Point out every Plasmodium parasite and every leukocyte.
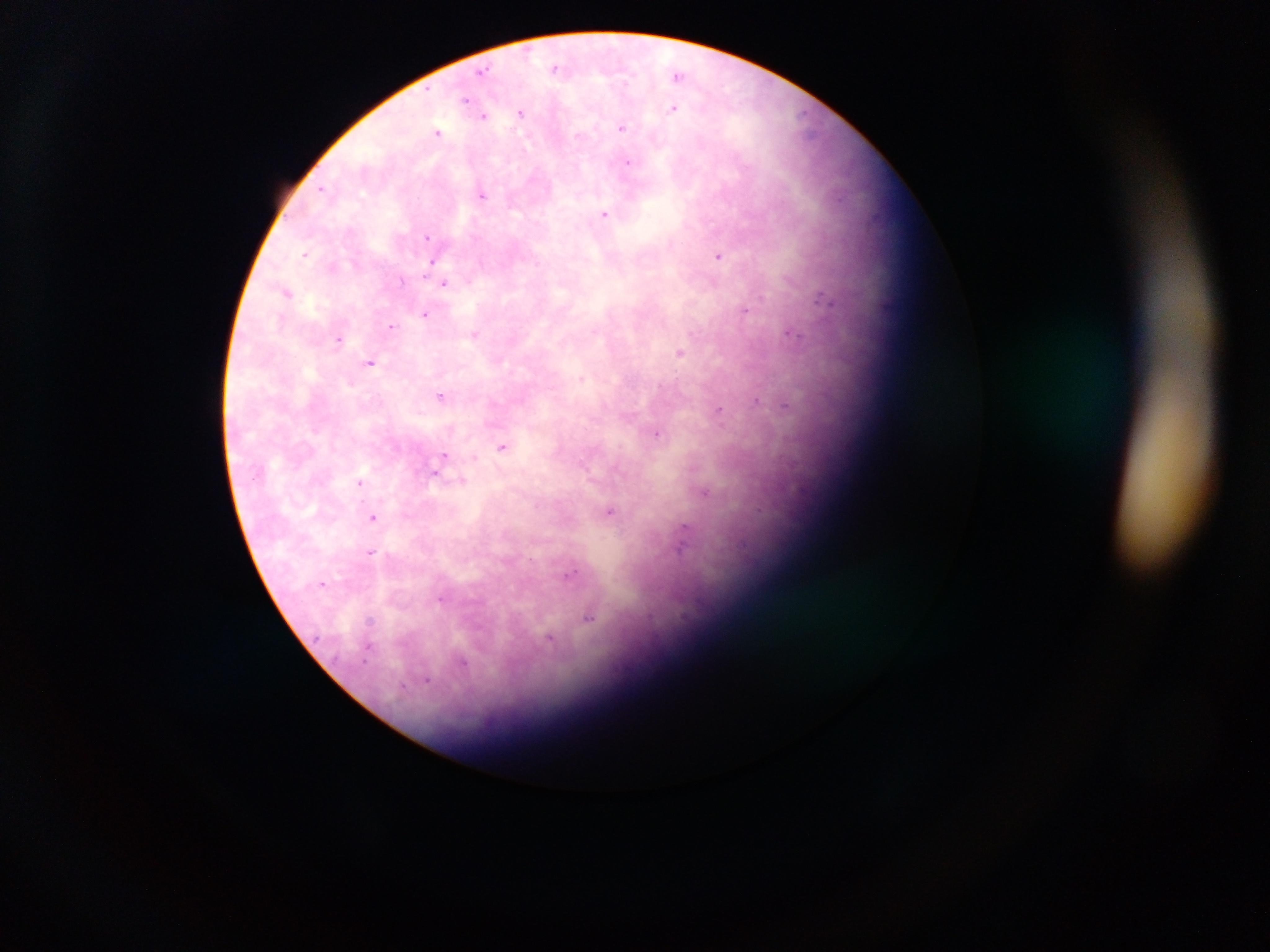

Approximate centers as {x, y} in pixels.
Plasmodium parasites: {555, 67}, {483, 71}, {677, 74}, {466, 100}, {673, 109}, {521, 113}, {484, 116}, {622, 128}, {438, 131}, {627, 161}, {323, 189}, {483, 195}, {604, 213}, {428, 237}, {305, 254}, {719, 256}, {431, 262}, {536, 263}, {426, 272}, {402, 280}, {444, 283}, {287, 292}, {762, 297}, {821, 297}, {745, 312}, {425, 314}, {391, 326}, {594, 331}, {791, 333}, {475, 334}, {339, 339}, {681, 352}, {370, 363}, {582, 379}, {441, 396}, {756, 400}, {786, 405}, {719, 411}, {658, 433}, {502, 447}, {475, 457}, {443, 459}, {435, 472}, {359, 481}, {462, 482}, {706, 492}, {610, 512}, {372, 517}, {683, 537}, {371, 552}, {571, 573}, {324, 583}, {441, 600}, {589, 617}, {370, 620}, {550, 641}, {368, 646}, {462, 664}, {428, 680}, {403, 686}.
No leukocytes observed.

{
  "image_size": "1270×952 pixels",
  "capture": "mobile-phone photograph through a microscope",
  "country": "Ghana",
  "preparation": "thick blood smear",
  "field_of_view": "single"
}